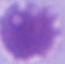 Captured at 1000x magnification. A red blood cell is seen. Photomicrograph.